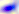
Summary:
  - Magnification: 400x
  - Modality: photomicrograph
  - Identification: Toxoplasma gondii